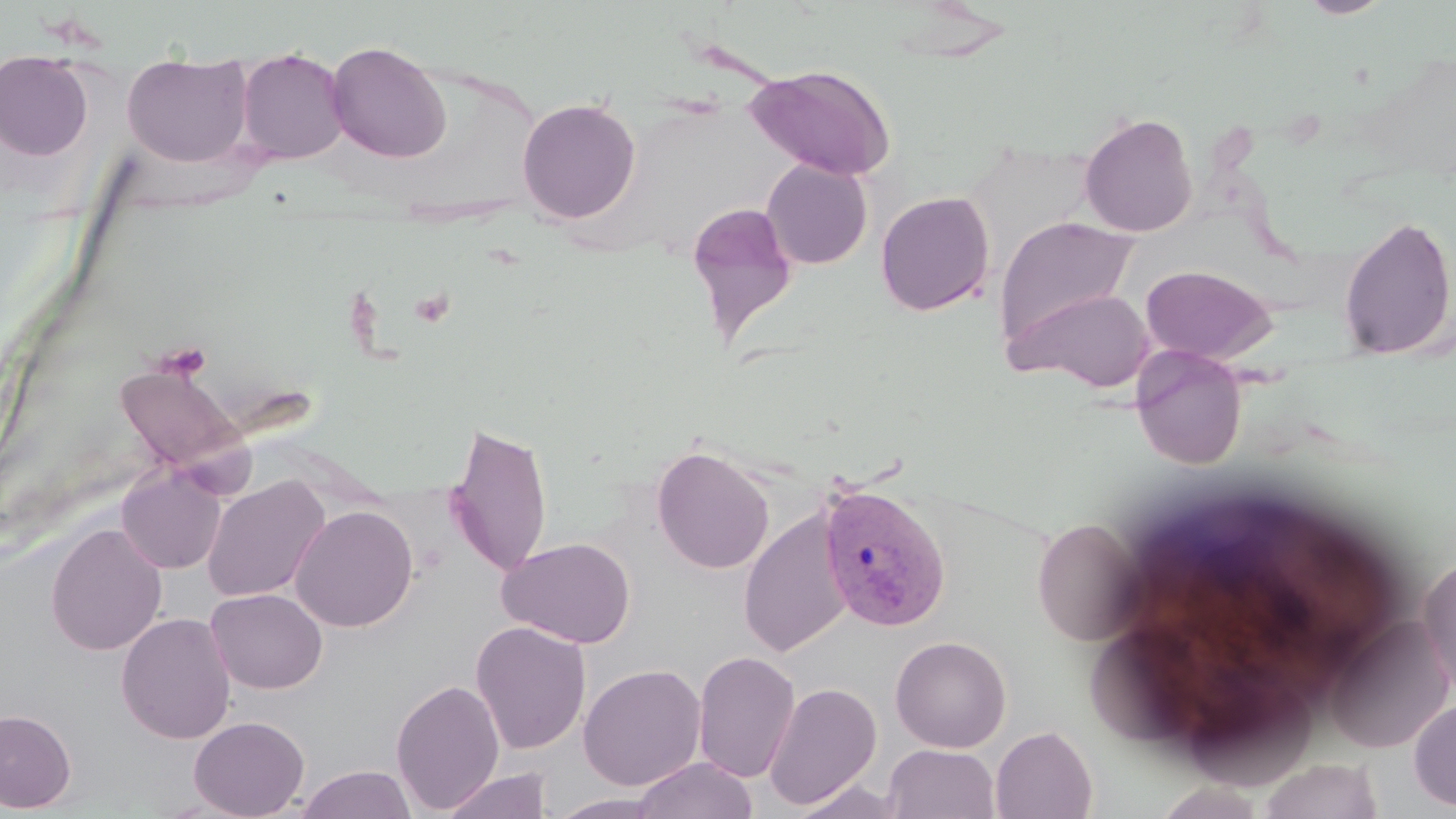

plasmodium_vivax_infected_red_blood_cell_locations: 'approximate bounding boxes as (x1,y1)-(x2,y2) corner pairs in pixels: (818,484)-(952,632)'
slide_level_diagnosis: Plasmodium vivax
magnification: 1000x
stain: May-Grünwald-Giemsa
modality: optical microscopy
uninfected_red_blood_cell_locations: 'approximate bounding boxes as (x1,y1)-(x2,y2) corner pairs in pixels: (1300,0)-(1391,18), (326,40)-(452,163), (236,47)-(349,164), (0,50)-(94,161), (122,56)-(253,167), (746,64)-(897,179), (517,97)-(641,224), (1079,113)-(1198,238), (761,159)-(873,269), (875,191)-(995,317), (685,201)-(799,348), (994,215)-(1141,347), (1338,215)-(1456,362), (1139,264)-(1276,365), (1007,286)-(1156,391), (1131,347)-(1247,469), (115,361)-(245,475), (445,419)-(553,578), (651,444)-(775,575), (117,466)-(226,574), (202,476)-(329,603), (290,505)-(418,632), (739,509)-(853,658), (1031,517)-(1147,645), (46,523)-(167,656), (498,536)-(637,648), (1418,550)-(1456,697), (206,588)-(327,694), (116,612)-(236,744), (1324,615)-(1453,753), (470,621)-(591,755), (890,635)-(1012,752), (692,650)-(800,783), (578,663)-(706,791), (391,678)-(505,814), (763,681)-(882,810), (1409,696)-(1456,813), (0,708)-(76,812), (188,715)-(310,818), (990,725)-(1097,819), (884,744)-(1000,819), (631,757)-(758,818), (1257,758)-(1385,819), (295,765)-(418,819), (440,768)-(553,819), (790,780)-(910,819), (1151,780)-(1268,819), (548,793)-(672,818)'
image_size: 1456×819 pixels
field_of_view: one of a larger specimen
platelet_locations: 'approximate bounding boxes as (x1,y1)-(x2,y2) corner pairs in pixels: (409,288)-(454,328), (153,341)-(211,380)'
preparation: thin blood film